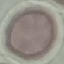 Result: no malaria parasites detected. Photographed with a smartphone camera at the microscope eyepiece. Giemsa stain. Automatically extracted cell patch, resized to 64 × 64 pixels. Thin blood film.